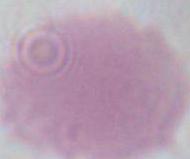
modality = micrograph
identification = erythrocyte
magnification = 1000x